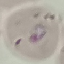
malaria status = parasitized
capture = smartphone through the microscope eyepiece
image type = automatically extracted cell patch, resized to 64 × 64 pixels
stain = Giemsa
preparation = thin blood film